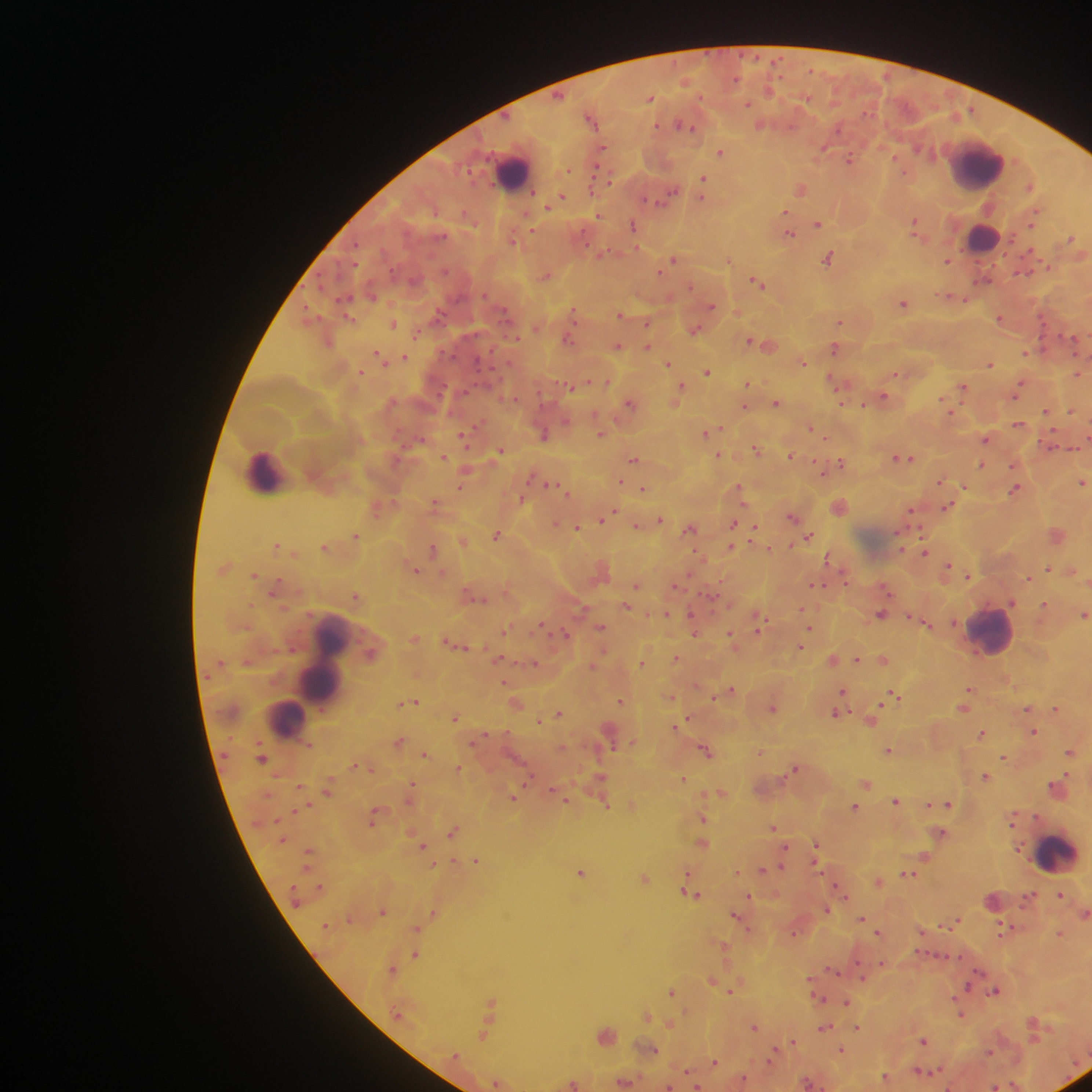

Approximate centers as x y in pixels.
Summary:
  - Malaria parasite locations: 650 98; 747 105; 592 117; 761 124; 685 125; 824 147; 602 148; 721 152; 849 158; 703 180; 802 188; 703 191; 662 198; 559 199; 553 201; 787 214; 598 216; 1033 219; 633 224; 818 224; 915 225; 789 233; 514 238; 1072 239; 829 257; 674 259; 728 260; 947 260; 545 275; 983 280; 757 282; 955 297; 904 303; 711 306; 574 311; 737 312; 439 314; 621 314; 348 317; 1000 318; 840 321; 648 323; 393 324; 695 329; 417 334; 1075 338; 569 339; 751 340; 328 341; 767 344; 617 346; 648 347; 835 348; 1027 352; 380 357; 404 357; 803 361; 668 363; 990 364; 361 371; 708 372; 1078 373; 897 374; 608 382; 836 382; 747 383; 574 387; 964 387; 1019 388; 680 389; 883 397; 677 398; 629 402; 777 402; 948 406; 745 407; 1072 410; 1047 411; 1019 424; 811 428; 708 431; 544 434; 601 434; 463 437; 825 438; 986 438; 757 449; 500 451; 719 455; 790 455; 444 457; 902 458; 634 459; 841 462; 981 464; 1015 465; 465 471; 822 471; 621 480; 940 480; 1083 482; 553 485; 963 486; 1016 488; 644 489; 740 489; 521 498; 435 502; 840 506; 948 506; 378 508; 912 511; 611 513; 607 516; 793 517; 660 519; 734 522; 556 524; 637 525; 578 528; 691 528; 754 530; 1057 533; 498 534; 356 535; 808 538; 464 542; 277 545; 325 546; 732 546; 769 548; 433 549; 925 552; 829 558; 225 567; 948 568; 1048 568; 416 570; 601 570; 1072 570; 255 575; 968 576; 1029 577; 636 585; 815 585; 675 586; 886 588; 274 589; 356 595; 712 596; 476 597; 1012 602; 626 606; 1045 606; 802 610; 882 613; 666 614; 1084 615; 761 622; 925 622; 694 623; 600 626; 810 627; 506 629; 694 631; 564 634; 731 637; 414 638; 457 643; 800 646; 677 657; 883 658; 501 659; 833 659; 856 659; 642 662; 533 663; 593 666; 730 690; 969 690; 843 691; 722 694; 671 696; 896 696; 621 700; 412 702; 516 703; 840 704; 773 707; 964 707; 1028 708; 1056 709; 559 713; 838 713; 455 717; 541 720; 687 720; 872 720; 682 724; 1034 732; 982 733; 611 739; 399 741; 707 750; 889 750; 760 751; 1070 751; 426 754; 1005 757; 262 758; 355 765; 369 767; 795 767; 459 768; 986 776; 601 777; 683 779; 866 783; 412 785; 301 787; 328 788; 553 789; 1058 789; 721 792; 558 794; 411 796; 513 798; 567 800; 897 800; 948 803; 633 804; 606 805; 930 805; 855 807; 373 818; 703 818; 1013 819; 774 827; 454 830; 942 833; 703 843; 817 843; 422 845; 786 848; 817 849; 925 856; 476 860; 454 861; 816 862; 434 864; 763 869; 582 872; 737 872; 909 874; 645 878; 878 880; 840 889; 691 894; 843 894; 1060 895; 749 897; 827 909; 383 910; 434 913; 1085 913; 738 916; 862 918; 956 920; 748 926; 418 928; 1003 929; 922 930; 794 932; 879 932; 1060 933; 724 945; 416 954; 883 963; 392 969; 834 971; 863 978; 713 979; 968 987; 732 990; 995 990; 672 991; 818 997; 954 997; 847 1001; 492 1002; 961 1014; 648 1016; 671 1025; 754 1025; 858 1027; 825 1028; 485 1033; 606 1034; 924 1040; 793 1041; 653 1050; 842 1050; 774 1052; 990 1052; 771 1060; 715 1061; 687 1071; 922 1071; 886 1076; 744 1078; 625 1080; 496 1082; 809 1082; 574 1083; 669 1086; 697 1086; 996 1086; 947 1087
  - Leukocyte locations: 977 165; 513 170; 983 237; 266 471; 991 631; 324 665; 285 719; 1058 852
  - Preparation: thick blood smear
  - Field of view: single
  - Image size: 1092×1092 pixels
  - Country: Ghana
  - Capture: mobile-phone photograph through a microscope